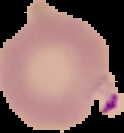
Summary:
  - Result: Plasmodium parasites detected
  - Image type: segmented cell region with the area outside set to black
  - Image size: 124×133 pixels
  - Preparation: thin blood smear